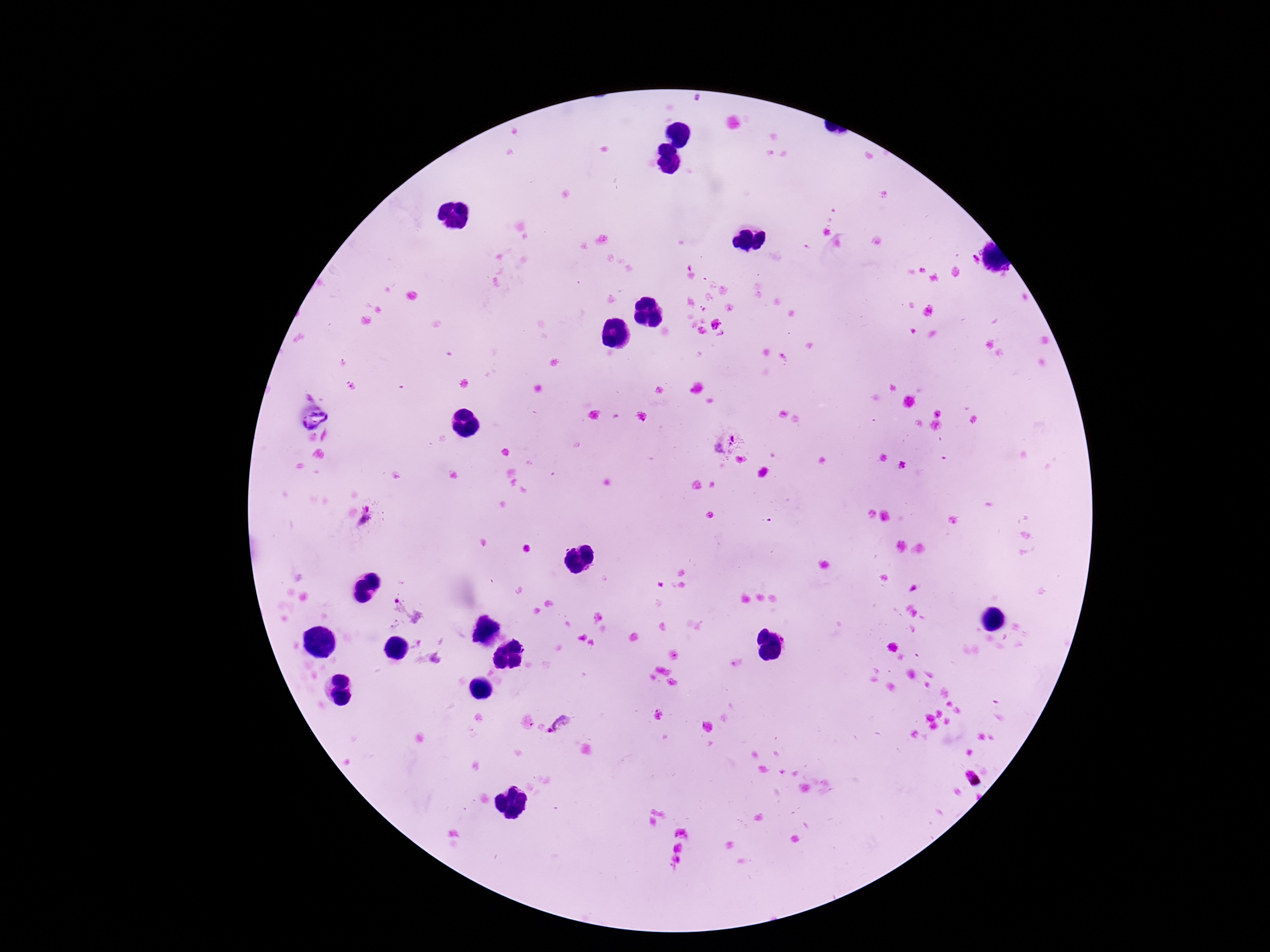

Approximate object centers, in pixels from the top-left corner.
Summary:
  - Plasmodium parasite locations: (x=721, y=441), (x=367, y=519), (x=408, y=611), (x=561, y=724)
  - Stain: Giemsa
  - Field of view: one from this slide
  - Magnification: 100x
  - Image size: 1270×952 pixels
  - Preparation: thick peripheral-blood smear
  - Capture: smartphone camera through the microscope eyepiece
  - Patient malaria status: infected